Locate every uninfected red blood cell.
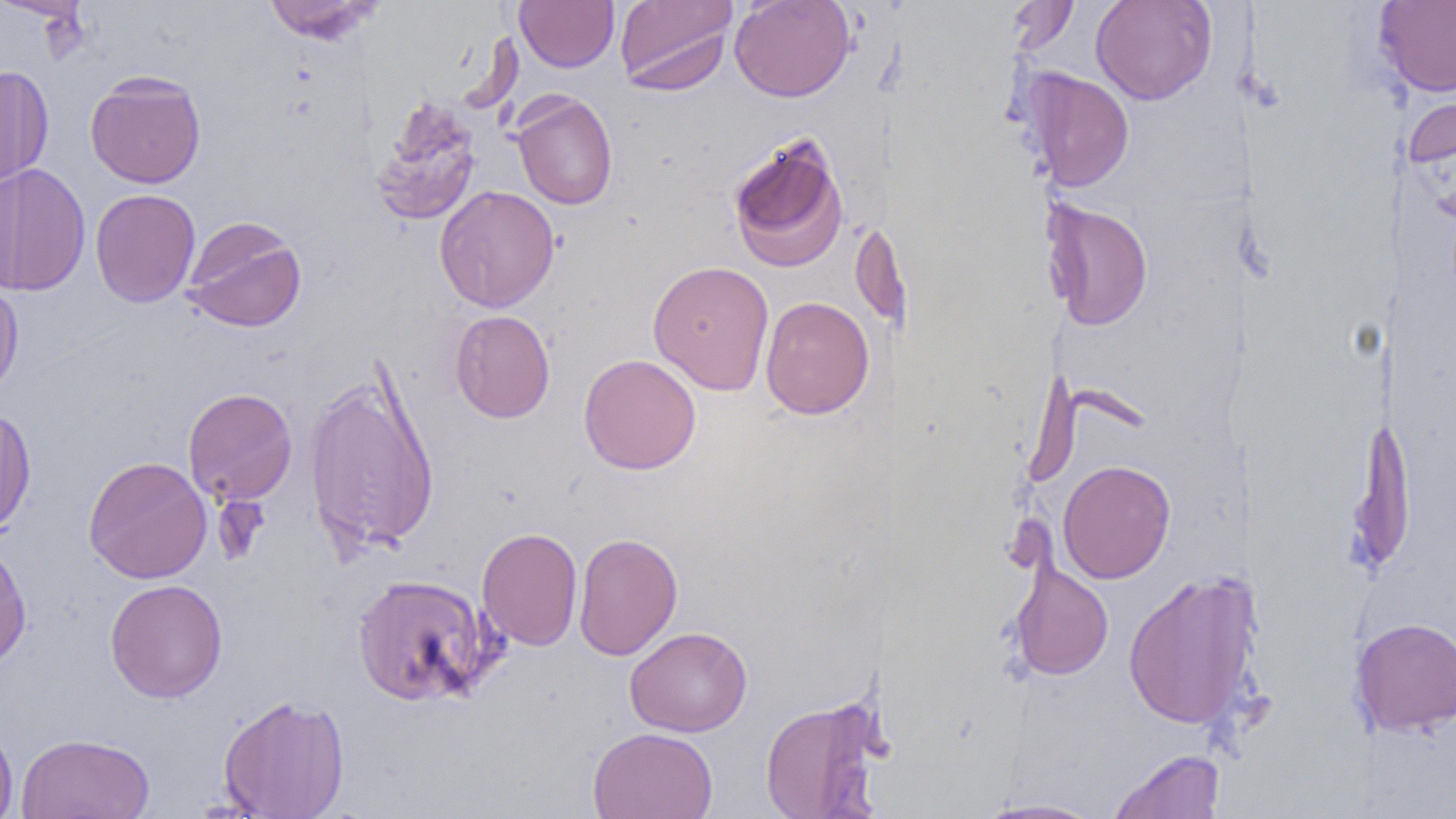

Approximate bounding boxes as named x1/y1/x2/y2 corners in pixels.
Uninfected red blood cells: (x1=0, y1=0, x2=93, y2=20), (x1=262, y1=0, x2=383, y2=44), (x1=515, y1=0, x2=619, y2=72), (x1=615, y1=0, x2=737, y2=94), (x1=729, y1=0, x2=856, y2=102), (x1=1008, y1=0, x2=1079, y2=56), (x1=1090, y1=0, x2=1217, y2=105), (x1=1373, y1=0, x2=1456, y2=98), (x1=0, y1=65, x2=54, y2=189), (x1=1023, y1=68, x2=1134, y2=192), (x1=84, y1=71, x2=206, y2=189), (x1=1402, y1=78, x2=1456, y2=177), (x1=512, y1=92, x2=618, y2=210), (x1=369, y1=97, x2=483, y2=226), (x1=727, y1=131, x2=850, y2=273), (x1=0, y1=163, x2=91, y2=297), (x1=0, y1=166, x2=20, y2=296), (x1=434, y1=185, x2=560, y2=313), (x1=89, y1=188, x2=201, y2=307), (x1=1042, y1=199, x2=1154, y2=331), (x1=888, y1=211, x2=913, y2=356), (x1=182, y1=216, x2=306, y2=333), (x1=852, y1=217, x2=889, y2=328), (x1=647, y1=260, x2=774, y2=395), (x1=0, y1=279, x2=24, y2=400), (x1=760, y1=296, x2=874, y2=419), (x1=450, y1=310, x2=555, y2=423), (x1=578, y1=353, x2=702, y2=474), (x1=303, y1=363, x2=441, y2=560), (x1=183, y1=387, x2=297, y2=506), (x1=0, y1=406, x2=36, y2=536), (x1=1346, y1=409, x2=1416, y2=577), (x1=83, y1=456, x2=212, y2=583), (x1=1058, y1=459, x2=1176, y2=584), (x1=477, y1=527, x2=583, y2=651), (x1=572, y1=532, x2=683, y2=661), (x1=0, y1=537, x2=32, y2=672), (x1=1010, y1=559, x2=1114, y2=681), (x1=1122, y1=571, x2=1255, y2=730), (x1=351, y1=573, x2=498, y2=707), (x1=105, y1=578, x2=228, y2=703), (x1=1349, y1=617, x2=1456, y2=737), (x1=625, y1=626, x2=752, y2=737), (x1=218, y1=693, x2=350, y2=819), (x1=759, y1=697, x2=885, y2=819), (x1=0, y1=723, x2=19, y2=819), (x1=587, y1=727, x2=719, y2=819), (x1=16, y1=732, x2=155, y2=818), (x1=1108, y1=748, x2=1226, y2=819), (x1=974, y1=797, x2=1108, y2=818).

Slide-level diagnosis: no evidence of blood parasites. Thin blood smear. One field of a larger specimen. Image is 1456×819 pixels. Captured at 1000x magnification. Light microscopy.